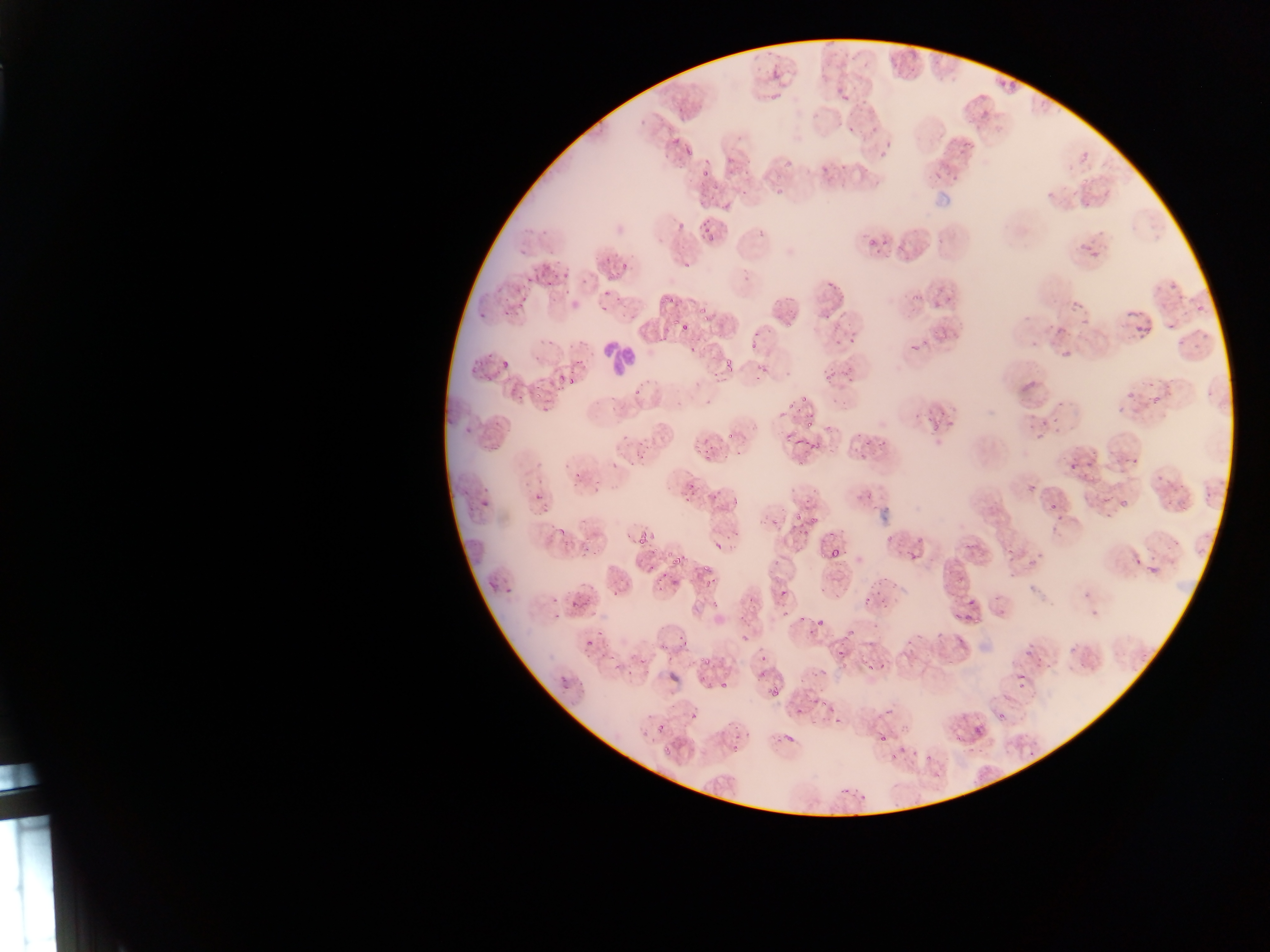
Approximate bounding boxes as left top right bottom in pixels. Malaria parasite locations: 895 51 916 71; 770 67 782 81; 994 70 1023 91; 836 84 851 104; 677 101 687 114; 976 101 997 120; 843 121 860 143; 962 129 978 149; 673 133 683 144; 683 144 693 163; 1080 152 1089 161; 818 158 830 175; 701 162 711 177; 701 220 718 237; 755 221 770 237; 1078 231 1097 254; 915 232 929 244; 866 234 876 258; 613 253 636 275; 548 261 569 283; 1159 266 1182 295; 822 273 835 287; 506 279 534 315; 1185 288 1212 309; 592 289 614 324; 1066 291 1094 313; 911 292 922 303; 1123 308 1140 324; 1136 322 1149 332; 1181 322 1206 348; 680 323 689 332; 832 334 845 348; 913 341 919 350; 1054 345 1074 364; 496 354 510 372; 720 354 736 376; 824 363 837 380; 553 371 573 389; 1008 371 1042 410; 1125 385 1153 412; 799 387 814 406; 1058 395 1067 407; 782 399 795 419; 460 416 471 435; 1035 423 1044 435; 794 428 832 462; 1120 445 1144 471; 1065 447 1084 467; 679 476 691 491; 708 482 732 506; 480 484 498 509; 533 491 542 502; 1113 495 1129 515; 1046 496 1059 517; 631 520 648 540; 824 541 841 563; 666 546 683 565; 1002 549 1011 560; 1136 557 1151 577; 568 577 599 610; 670 578 680 587; 867 578 884 595; 774 583 790 602; 961 602 975 619; 815 617 822 626; 935 625 948 644; 836 628 861 654; 582 632 600 651; 866 643 889 671; 669 653 688 684; 1014 659 1030 690; 557 674 571 691; 721 682 727 690; 770 688 778 696; 796 696 823 720; 727 713 758 754; 871 719 899 749; 657 722 667 732; 967 724 981 752; 642 730 651 739; 788 730 800 745; 890 734 914 763; 922 746 941 770; 844 779 865 807. Leukocyte locations: 599 339 633 380. Image is 1270×952 pixels. Sample from Ghana. Thin blood film. Single field of view. Photographed through a microscope with a mobile-phone camera.